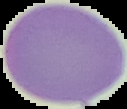

Summary:
  - Malaria status: uninfected
  - Image size: 127×109 pixels
  - Preparation: thin blood smear
  - Image type: segmented cell region on a black background